State which cell type is depicted.
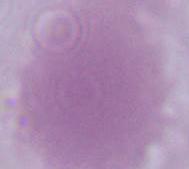
An erythrocyte.

Captured at 1000x magnification. Photomicrograph.